Identify the preparation type.
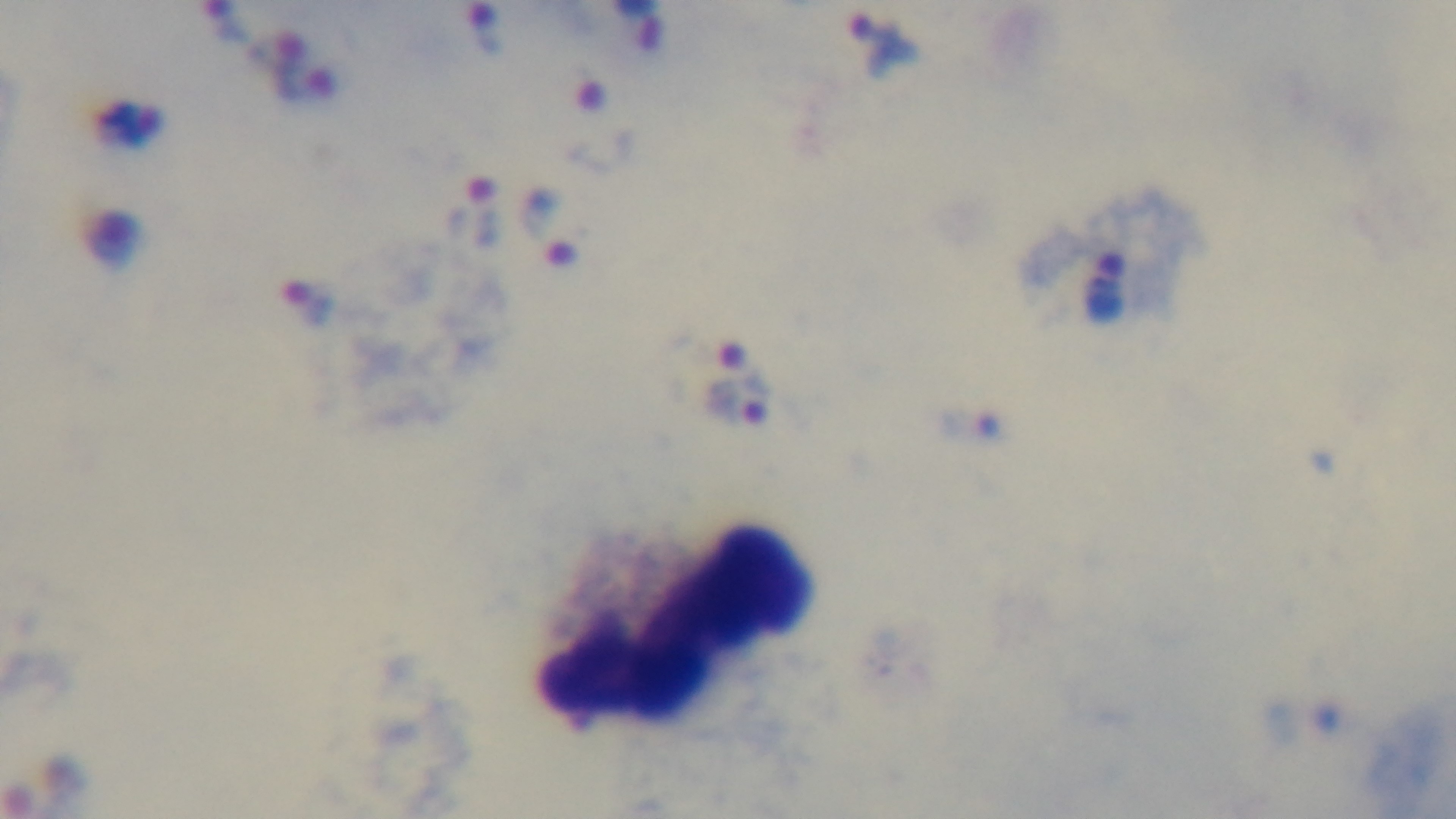

It is a thick blood film.

field of view = single
malaria status = positive
capture = mounted 4K digital camera
stain = Giemsa
objective = 100x oil immersion
modality = light microscopy